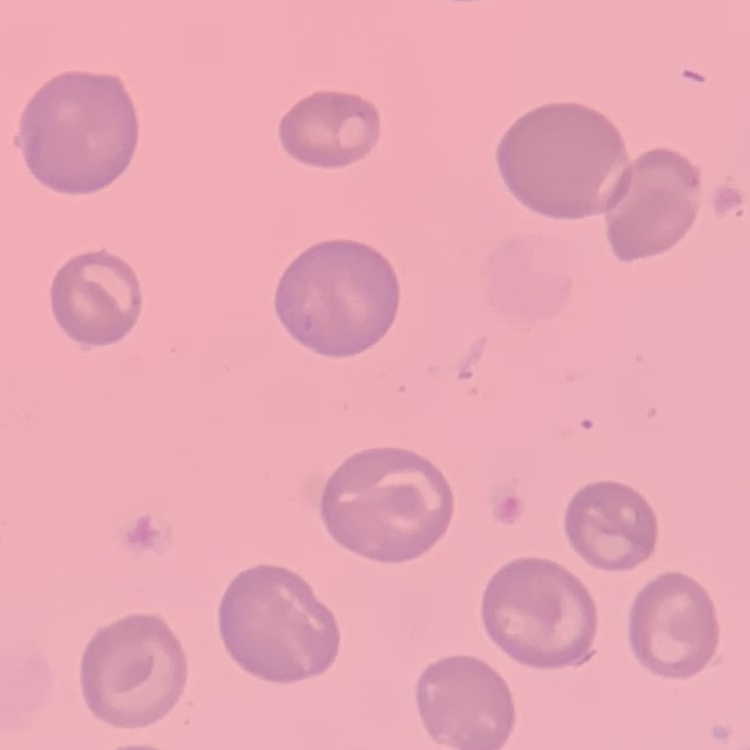

Summary:
  - Erythrocyte morphology: no rouleaux formation
  - Stain: Field's or Giemsa
  - Preparation: thin blood smear
  - Image type: one tile cut from a larger photomicrograph